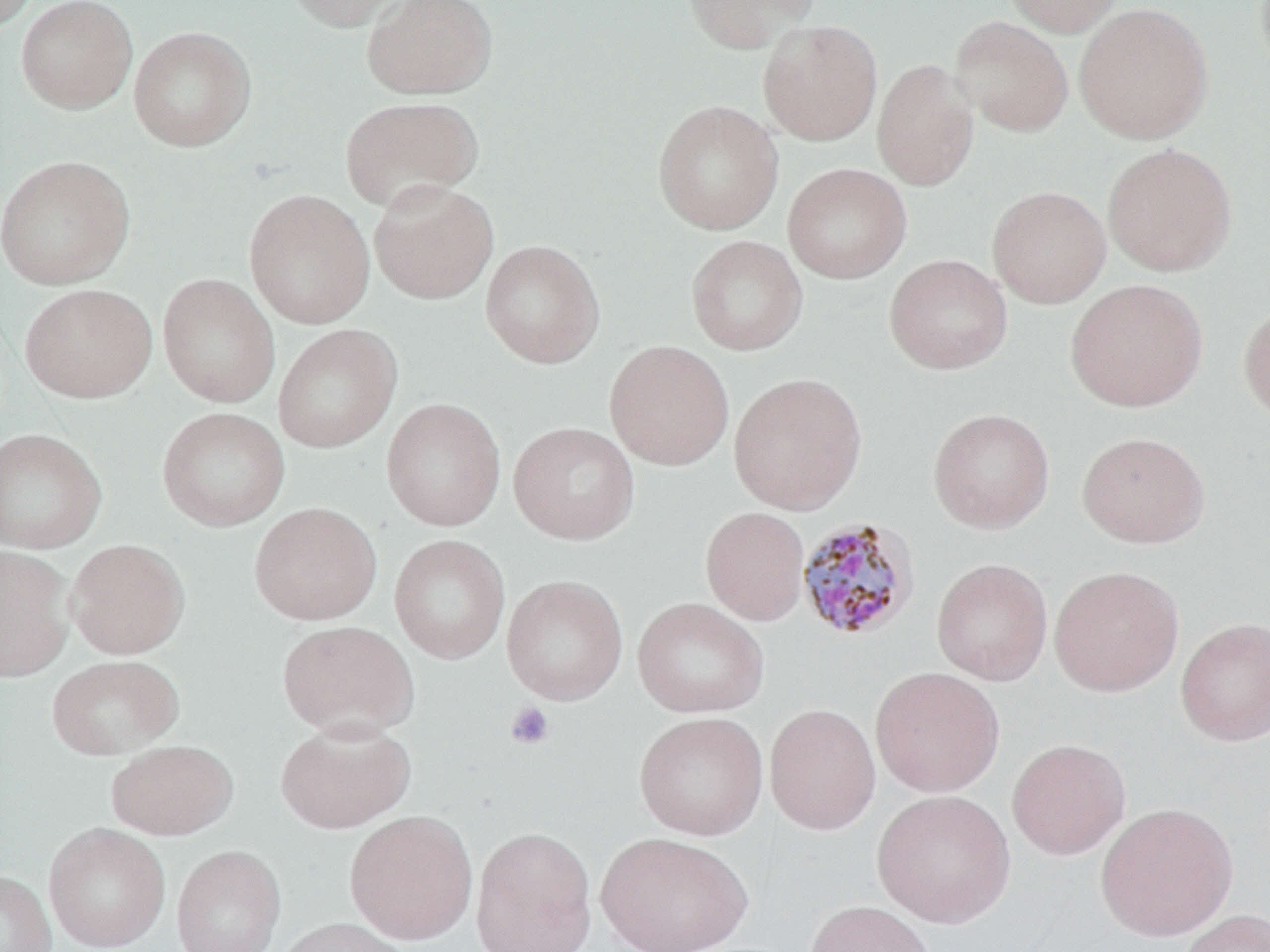
slide-level diagnosis = Plasmodium malariae
preparation = thin blood smear
Plasmodium malariae-infected red blood cell locations = approximate bounding boxes as (x1,y1)-(x2,y2) corner pairs in pixels: (796,516)-(921,641)
uninfected red blood cell locations = approximate bounding boxes as (x1,y1)-(x2,y2) corner pairs in pixels: (1,0)-(39,35), (15,0)-(138,113), (283,0)-(417,32), (361,0)-(498,101), (679,0)-(819,53), (1001,0)-(1126,37), (1073,2)-(1214,145), (950,16)-(1074,137), (757,20)-(883,145), (128,25)-(256,152), (872,58)-(980,191), (339,95)-(485,213), (651,99)-(784,236), (1101,142)-(1238,277), (1,155)-(135,289), (782,163)-(912,284), (368,178)-(500,304), (986,185)-(1111,308), (243,189)-(375,329), (685,235)-(808,356), (480,239)-(605,368), (883,253)-(1013,375), (157,273)-(281,408), (1065,278)-(1208,412), (19,283)-(157,403), (1237,301)-(1270,426), (271,324)-(402,454), (603,340)-(734,471), (727,371)-(868,515), (380,397)-(506,532), (156,406)-(290,531), (927,407)-(1055,534), (508,422)-(640,545), (0,428)-(107,554), (1076,431)-(1211,548), (249,501)-(382,625), (700,506)-(810,625), (389,533)-(511,665), (65,539)-(190,659), (0,546)-(75,683), (931,557)-(1053,685), (1048,565)-(1184,697), (500,574)-(629,705), (631,596)-(770,719), (1175,616)-(1270,746), (277,620)-(419,739), (46,654)-(184,760), (869,667)-(1005,797), (764,703)-(882,835), (633,711)-(769,840), (274,718)-(417,834), (1006,738)-(1131,859), (106,739)-(238,840), (871,789)-(1016,928), (1094,801)-(1238,941), (344,810)-(478,944), (43,822)-(170,952), (470,825)-(598,951), (595,831)-(753,952), (170,844)-(286,952), (0,870)-(57,952), (803,899)-(936,952), (1176,907)-(1269,952), (273,917)-(413,952)
modality = light microscopy
stain = May-Grünwald-Giemsa
platelet locations = approximate bounding boxes as (x1,y1)-(x2,y2) corner pairs in pixels: (505,702)-(555,750)
magnification = 1000x
image size = 1270×952 pixels
field of view = one of a larger specimen